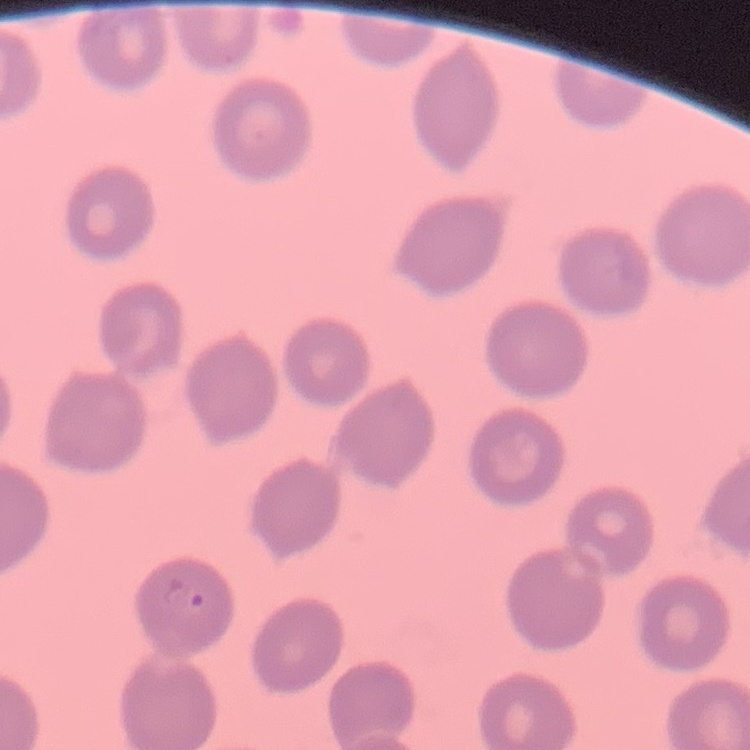
red blood cell morphology = no rouleaux formation
image type = one tile cut from a larger photomicrograph
preparation = thin blood film
stain = Field's or Giemsa